Assess this cell for malaria.
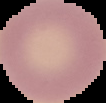
It is uninfected.

image type = segmented cell region on a black background
image size = 106×103 pixels
preparation = thin blood film